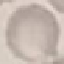
Summary:
  - Malaria status: uninfected
  - Stain: Giemsa
  - Preparation: thin blood film
  - Image type: automatically extracted cell patch, resized to 64 × 64 pixels
  - Capture: smartphone through the microscope eyepiece